State the blood parasite species.
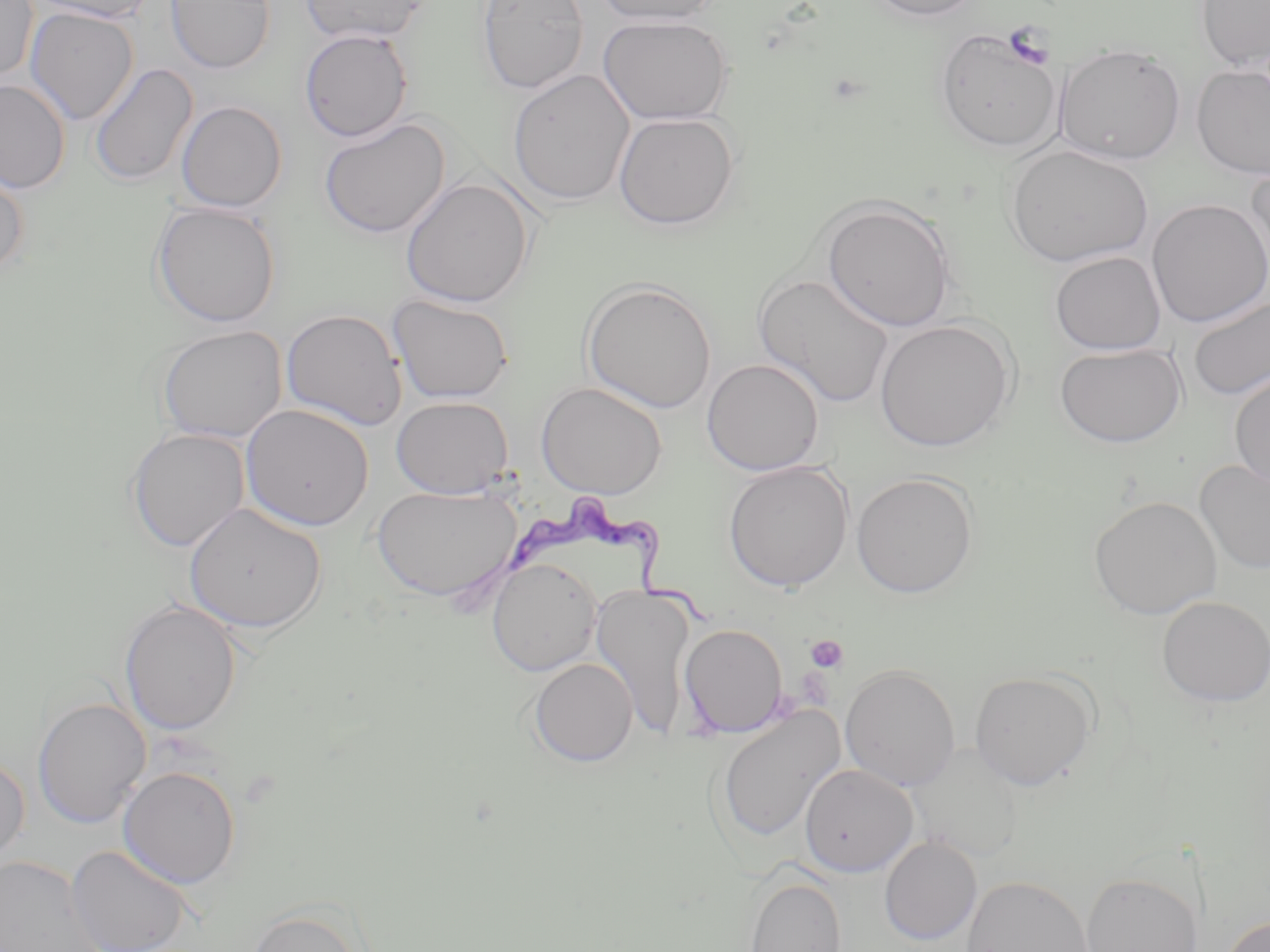

Trypanosoma brucei.

Summary:
  - Coordinate format: approximate bounding boxes as named x1/y1/x2/y2 corners in pixels
  - Uninfected red blood cell locations: (x1=0, y1=0, x2=37, y2=83), (x1=27, y1=0, x2=155, y2=23), (x1=165, y1=0, x2=276, y2=73), (x1=301, y1=0, x2=431, y2=44), (x1=476, y1=0, x2=589, y2=94), (x1=594, y1=0, x2=723, y2=26), (x1=867, y1=0, x2=983, y2=20), (x1=1196, y1=0, x2=1270, y2=69), (x1=25, y1=7, x2=138, y2=125), (x1=597, y1=14, x2=734, y2=125), (x1=934, y1=25, x2=1063, y2=153), (x1=299, y1=28, x2=413, y2=142), (x1=1054, y1=42, x2=1186, y2=165), (x1=89, y1=63, x2=198, y2=187), (x1=1191, y1=64, x2=1270, y2=180), (x1=507, y1=68, x2=635, y2=207), (x1=0, y1=78, x2=70, y2=194), (x1=176, y1=100, x2=287, y2=212), (x1=613, y1=111, x2=740, y2=231), (x1=318, y1=117, x2=450, y2=239), (x1=1003, y1=144, x2=1154, y2=268), (x1=1244, y1=160, x2=1270, y2=289), (x1=0, y1=166, x2=30, y2=277), (x1=400, y1=177, x2=534, y2=308), (x1=820, y1=197, x2=958, y2=332), (x1=1146, y1=198, x2=1270, y2=327), (x1=151, y1=201, x2=281, y2=328), (x1=1050, y1=251, x2=1166, y2=355), (x1=755, y1=273, x2=895, y2=408), (x1=581, y1=278, x2=718, y2=413), (x1=1186, y1=294, x2=1270, y2=402), (x1=387, y1=295, x2=515, y2=404), (x1=281, y1=308, x2=408, y2=431), (x1=874, y1=318, x2=1017, y2=451), (x1=156, y1=325, x2=288, y2=444), (x1=1054, y1=342, x2=1186, y2=448), (x1=701, y1=358, x2=825, y2=475), (x1=1230, y1=370, x2=1270, y2=489), (x1=536, y1=381, x2=667, y2=498), (x1=391, y1=396, x2=513, y2=498), (x1=241, y1=404, x2=375, y2=531), (x1=126, y1=427, x2=250, y2=552), (x1=1194, y1=458, x2=1270, y2=575), (x1=723, y1=460, x2=853, y2=592), (x1=851, y1=471, x2=979, y2=598), (x1=371, y1=483, x2=522, y2=602), (x1=1089, y1=495, x2=1222, y2=619), (x1=184, y1=502, x2=326, y2=635), (x1=486, y1=557, x2=602, y2=676), (x1=591, y1=583, x2=697, y2=737), (x1=1156, y1=595, x2=1270, y2=707), (x1=119, y1=599, x2=242, y2=736), (x1=679, y1=623, x2=788, y2=737), (x1=528, y1=657, x2=638, y2=767), (x1=840, y1=664, x2=961, y2=790), (x1=969, y1=669, x2=1097, y2=790), (x1=32, y1=696, x2=151, y2=828), (x1=715, y1=705, x2=845, y2=845), (x1=908, y1=744, x2=1025, y2=862), (x1=0, y1=755, x2=30, y2=869), (x1=799, y1=763, x2=918, y2=877), (x1=118, y1=766, x2=241, y2=889), (x1=879, y1=837, x2=982, y2=945), (x1=66, y1=845, x2=194, y2=952), (x1=0, y1=855, x2=104, y2=952), (x1=1080, y1=871, x2=1203, y2=952), (x1=962, y1=874, x2=1093, y2=952), (x1=744, y1=875, x2=847, y2=952), (x1=245, y1=905, x2=367, y2=952), (x1=1220, y1=914, x2=1270, y2=952)
  - Platelet locations: (x1=1003, y1=22, x2=1053, y2=70), (x1=805, y1=634, x2=849, y2=673)
  - Trypanosoma brucei locations: (x1=501, y1=499, x2=719, y2=628)
  - Field of view: one of a larger specimen
  - Preparation: thin blood film
  - Modality: optical microscopy
  - Image size: 1270×952 pixels
  - Stain: May-Grünwald-Giemsa
  - Magnification: 1000x